Assess the background quality.
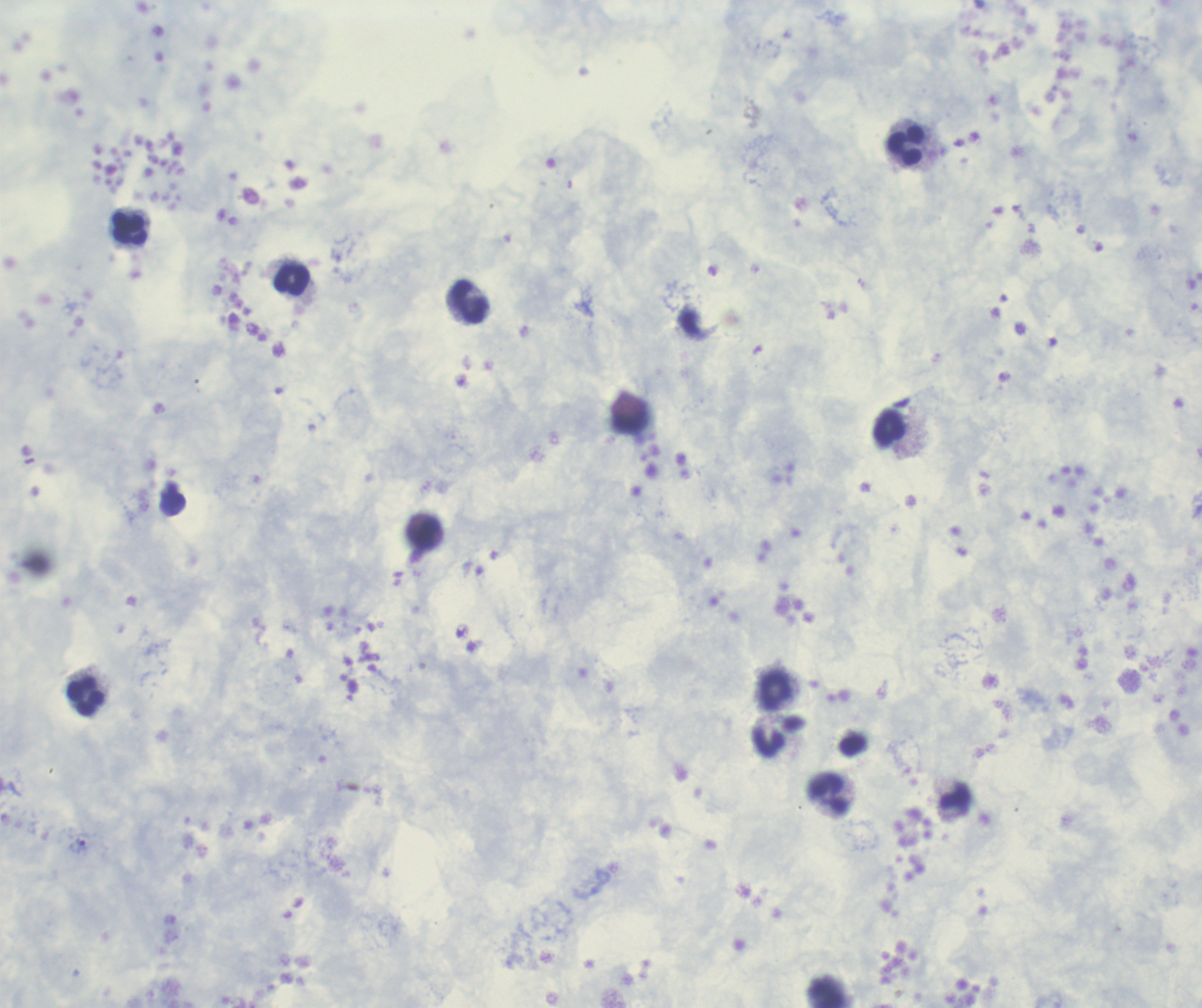
It is good.

Approximate centers as {x, y} in pixels. Leukocyte locations: {905, 147}, {129, 229}, {292, 280}, {470, 303}, {632, 420}, {891, 429}, {426, 535}, {775, 691}, {86, 697}, {778, 736}, {828, 795}. Trophozoite locations: {77, 846}. Single field of view. 100x magnification. Coloration quality: good. Image is 1202×1008 pixels. Romanowsky stain. Thick blood smear. Previously used in an actual diagnosis. Result: malaria parasites detected.